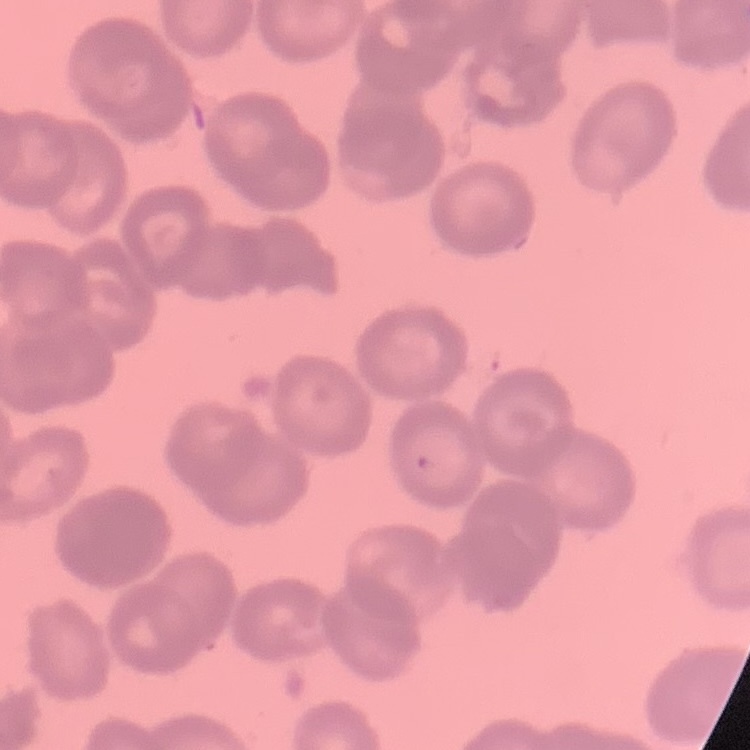
red blood cell morphology = rouleaux formation
stain = Field's or Giemsa
image type = square crop of a larger photomicrograph
preparation = thin peripheral smear